Classify this cell by malaria status.
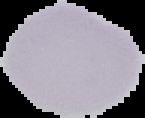
It is uninfected.

Summary:
  - Image size: 145×118 pixels
  - Preparation: thin blood film
  - Image type: segmented cell region with the area outside set to black